Outline each Plasmodium vivax-infected red blood cell.
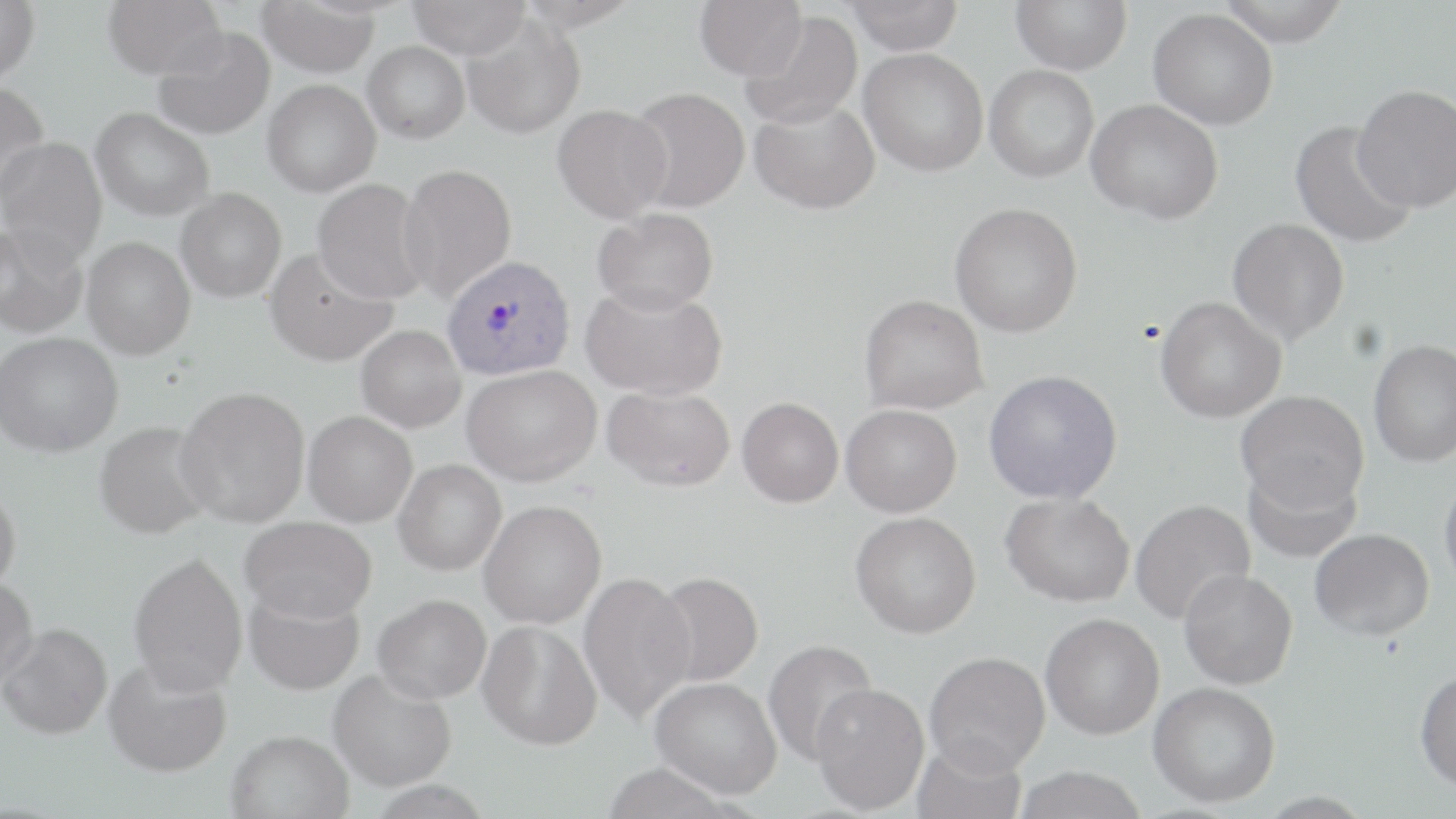
Approximate bounding boxes as [x1, y1, x2, y2] in pixels.
Plasmodium vivax-infected red blood cells: [441, 254, 576, 381].

Uninfected red blood cell locations: [0, 0, 40, 85], [102, 0, 226, 79], [407, 0, 532, 60], [516, 0, 642, 31], [846, 0, 964, 55], [1011, 0, 1131, 74], [1218, 0, 1348, 47], [257, 1, 381, 77], [693, 1, 805, 79], [1148, 8, 1278, 130], [739, 11, 863, 129], [461, 15, 586, 139], [152, 27, 275, 139], [362, 41, 470, 143], [859, 48, 988, 176], [984, 65, 1098, 182], [262, 79, 380, 197], [0, 81, 49, 202], [1353, 84, 1456, 211], [626, 86, 751, 213], [749, 98, 880, 214], [1086, 99, 1224, 224], [551, 103, 672, 223], [90, 107, 215, 221], [1290, 121, 1417, 250], [0, 136, 107, 262], [398, 163, 517, 301], [311, 179, 431, 304], [175, 188, 286, 302], [949, 202, 1082, 337], [593, 207, 718, 316], [1227, 218, 1349, 345], [0, 220, 88, 339], [82, 237, 195, 360], [264, 247, 398, 367], [580, 283, 727, 400], [859, 293, 988, 415], [1155, 296, 1286, 423], [355, 325, 465, 433], [0, 331, 122, 457], [1368, 340, 1456, 467], [462, 364, 601, 486], [983, 369, 1122, 504], [602, 385, 735, 491], [176, 386, 310, 527], [1236, 389, 1370, 513], [737, 397, 843, 507], [841, 403, 962, 517], [303, 411, 417, 526], [94, 420, 214, 539], [393, 459, 506, 575], [1242, 461, 1362, 564], [1439, 470, 1456, 596], [0, 486, 21, 594], [1001, 492, 1135, 606], [1130, 498, 1255, 624], [478, 500, 606, 628], [850, 511, 981, 638], [240, 516, 376, 623], [1309, 528, 1434, 640], [128, 551, 248, 694], [1178, 569, 1298, 689], [578, 571, 696, 724], [653, 571, 764, 687], [0, 577, 37, 687], [243, 588, 365, 696], [372, 593, 491, 703], [1040, 612, 1165, 739], [478, 619, 602, 751], [1, 622, 112, 739], [762, 639, 879, 767], [924, 651, 1050, 776], [103, 657, 232, 777], [328, 669, 456, 792], [1414, 669, 1456, 792], [650, 676, 781, 799], [1148, 681, 1280, 808], [811, 682, 930, 814], [226, 730, 353, 819], [911, 737, 1028, 819], [601, 763, 744, 819], [1013, 765, 1150, 819], [365, 781, 496, 818]. Slide-level diagnosis: Plasmodium vivax. Optical microscopy. Image is 1456×819 pixels. Captured at 1000x magnification. Single field of view. Thin blood smear. May-Grünwald-Giemsa-stained preparation.